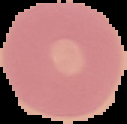
preparation: thin blood smear
image_type: segmented cell region on a black background
image_size: 127×124 pixels
result: negative for Plasmodium parasites